Identify the parasite.
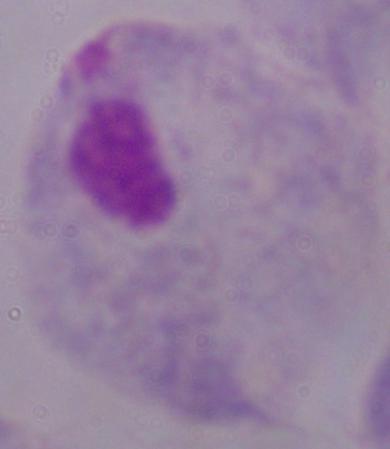
A trichomonad.

Captured at 1000x magnification. Micrograph.